Classify this cell by malaria status.
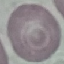

Uninfected.

capture: smartphone through the microscope eyepiece
image_type: automatically extracted cell patch, resized to 64 × 64 pixels
stain: Giemsa
preparation: thin blood film